Assess this cell for malaria.
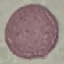

It is uninfected.

Giemsa stain. Thin smear of blood. Automatically extracted cell patch, resized to 64 × 64 pixels. Acquired by smartphone through the microscope eyepiece.